State which parasite is depicted.
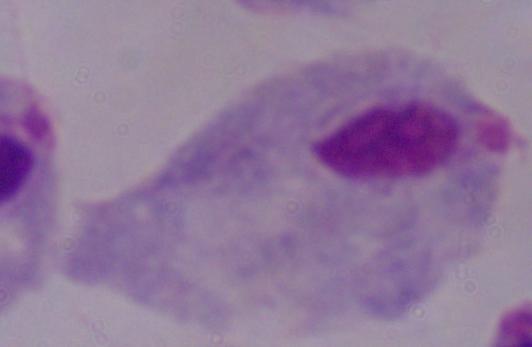
A trichomonad.

Captured at 1000x magnification. Micrograph.